State the blood parasite species.
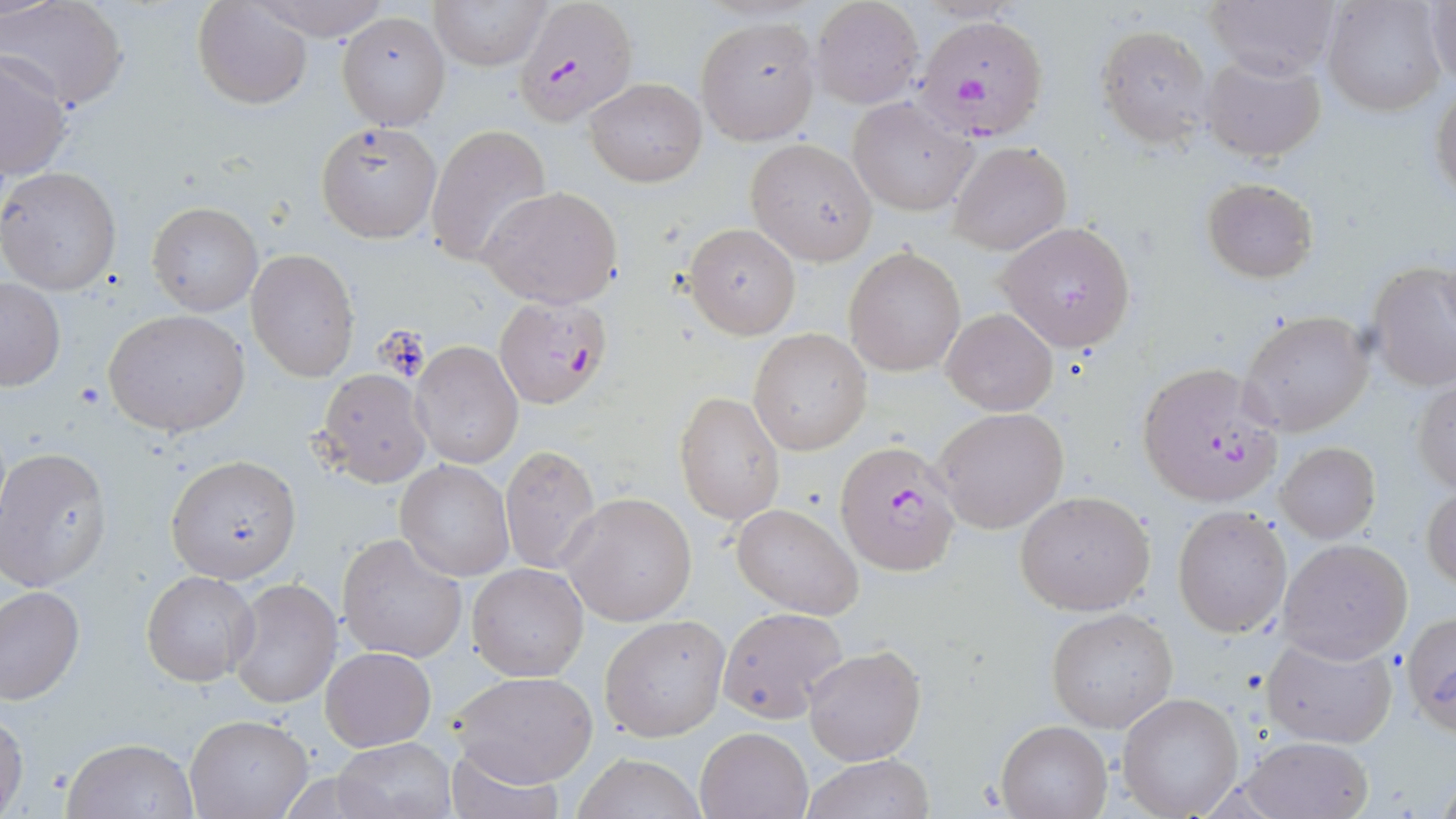
Plasmodium falciparum.

{
  "magnification": "1000x",
  "uninfected_red_blood_cell_locations": "approximate bounding boxes as named x1/y1/x2/y2 corners in pixels: (x1=2, y1=0, x2=128, y2=111), (x1=192, y1=0, x2=311, y2=109), (x1=249, y1=0, x2=395, y2=42), (x1=430, y1=0, x2=556, y2=70), (x1=1203, y1=0, x2=1340, y2=79), (x1=1321, y1=0, x2=1448, y2=116), (x1=1425, y1=0, x2=1456, y2=85), (x1=809, y1=1, x2=924, y2=108), (x1=337, y1=10, x2=449, y2=129), (x1=696, y1=15, x2=821, y2=146), (x1=1097, y1=25, x2=1213, y2=147), (x1=1, y1=52, x2=74, y2=178), (x1=1200, y1=56, x2=1325, y2=161), (x1=583, y1=76, x2=706, y2=186), (x1=1431, y1=87, x2=1456, y2=205), (x1=848, y1=98, x2=976, y2=216), (x1=316, y1=121, x2=441, y2=242), (x1=427, y1=125, x2=551, y2=267), (x1=746, y1=138, x2=878, y2=265), (x1=948, y1=142, x2=1071, y2=254), (x1=0, y1=166, x2=121, y2=295), (x1=1201, y1=178, x2=1317, y2=281), (x1=478, y1=185, x2=624, y2=308), (x1=148, y1=202, x2=262, y2=316), (x1=996, y1=221, x2=1137, y2=351), (x1=683, y1=222, x2=801, y2=338), (x1=844, y1=245, x2=966, y2=378), (x1=246, y1=250, x2=359, y2=380), (x1=1366, y1=261, x2=1456, y2=391), (x1=0, y1=277, x2=65, y2=391), (x1=941, y1=308, x2=1057, y2=416), (x1=103, y1=309, x2=249, y2=437), (x1=1238, y1=311, x2=1375, y2=436), (x1=749, y1=329, x2=872, y2=456), (x1=410, y1=340, x2=523, y2=470), (x1=316, y1=368, x2=432, y2=487), (x1=1413, y1=375, x2=1456, y2=495), (x1=674, y1=391, x2=785, y2=527), (x1=935, y1=407, x2=1070, y2=535), (x1=1276, y1=442, x2=1380, y2=544), (x1=500, y1=444, x2=601, y2=575), (x1=0, y1=446, x2=112, y2=592), (x1=166, y1=455, x2=301, y2=583), (x1=397, y1=459, x2=513, y2=581), (x1=1423, y1=483, x2=1455, y2=593), (x1=1014, y1=490, x2=1155, y2=615), (x1=563, y1=493, x2=697, y2=625), (x1=732, y1=502, x2=863, y2=619), (x1=1172, y1=506, x2=1292, y2=638), (x1=338, y1=533, x2=468, y2=662), (x1=1278, y1=539, x2=1413, y2=663), (x1=467, y1=564, x2=590, y2=682), (x1=141, y1=569, x2=257, y2=685), (x1=227, y1=578, x2=341, y2=709), (x1=0, y1=584, x2=84, y2=704), (x1=719, y1=607, x2=853, y2=724), (x1=1046, y1=608, x2=1179, y2=733), (x1=1402, y1=611, x2=1456, y2=733), (x1=599, y1=614, x2=730, y2=741), (x1=1261, y1=633, x2=1399, y2=749), (x1=803, y1=645, x2=926, y2=766), (x1=322, y1=647, x2=435, y2=751), (x1=449, y1=671, x2=599, y2=789), (x1=1117, y1=692, x2=1246, y2=818), (x1=0, y1=709, x2=27, y2=817), (x1=185, y1=715, x2=311, y2=819), (x1=995, y1=720, x2=1112, y2=819), (x1=694, y1=726, x2=812, y2=819), (x1=1240, y1=735, x2=1372, y2=819), (x1=63, y1=737, x2=198, y2=818), (x1=333, y1=737, x2=458, y2=819), (x1=441, y1=745, x2=564, y2=819), (x1=572, y1=752, x2=708, y2=819), (x1=796, y1=754, x2=934, y2=819)",
  "field_of_view": "one of a larger specimen",
  "preparation": "thin blood smear",
  "plasmodium_falciparum_infected_red_blood_cell_locations": "approximate bounding boxes as named x1/y1/x2/y2 corners in pixels: (x1=513, y1=1, x2=637, y2=127), (x1=913, y1=17, x2=1046, y2=140), (x1=493, y1=293, x2=615, y2=409), (x1=1136, y1=361, x2=1286, y2=507), (x1=834, y1=439, x2=963, y2=576)",
  "image_size": "1456×819 pixels",
  "modality": "light microscopy",
  "stain": "May-Grünwald-Giemsa"
}